Outline each Plasmodium vivax-infected red blood cell.
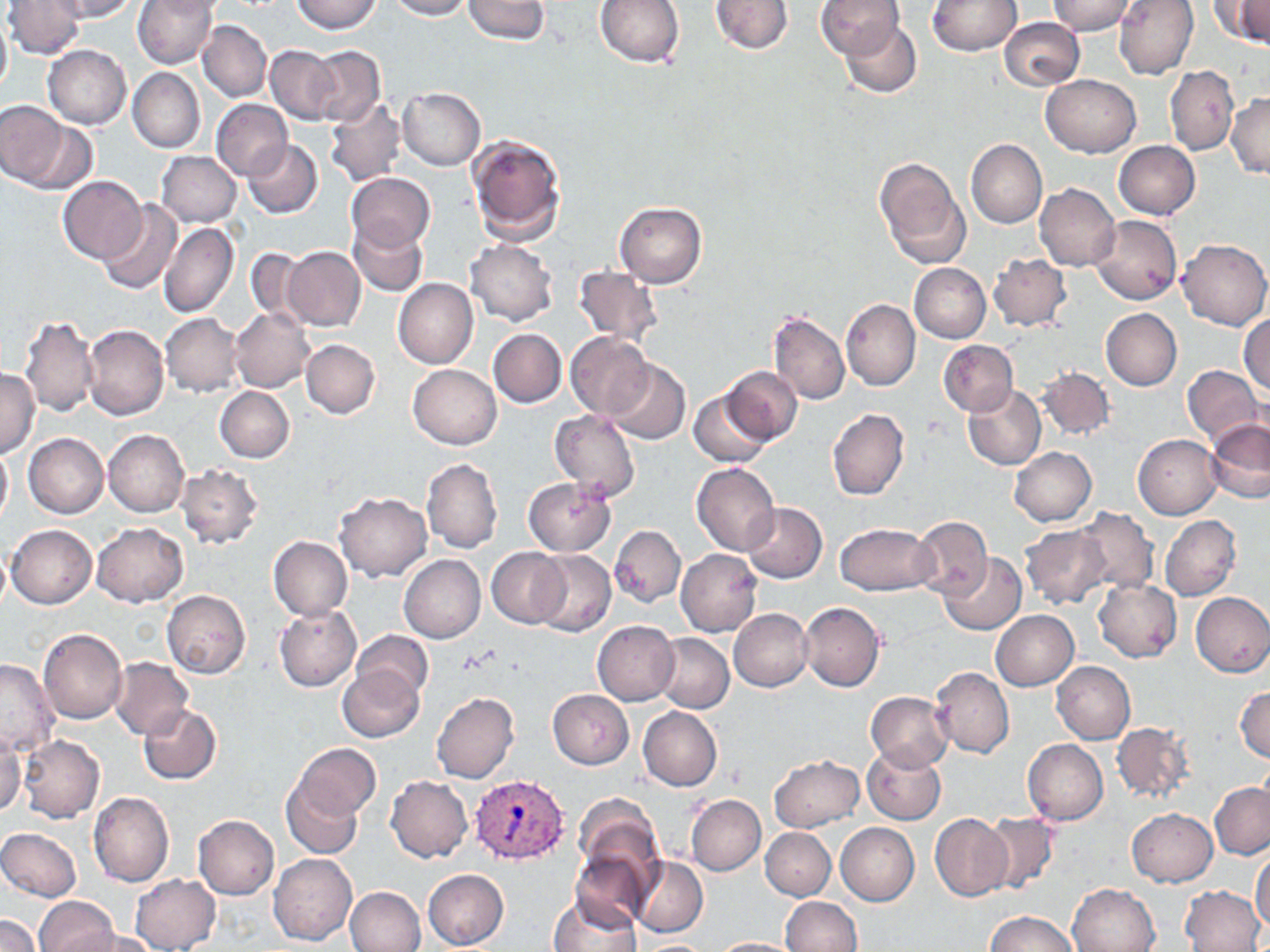

Approximate bounding boxes as (x1,y1)-(x2,y2) corner pairs in pixels.
Plasmodium vivax-infected red blood cells: (470,775)-(570,866).

slide-level diagnosis = Plasmodium vivax
modality = light microscopy
field of view = single
preparation = thin blood smear
uninfected red blood cell locations = approximate bounding boxes as (x1,y1)-(x2,y2) corner pairs in pixels: (4,0)-(84,58), (57,0)-(141,21), (133,0)-(218,69), (290,0)-(381,33), (388,0)-(472,20), (463,0)-(548,43), (595,0)-(685,68), (710,0)-(794,55), (816,0)-(906,59), (927,0)-(1021,55), (1114,0)-(1199,79), (1214,0)-(1270,46), (1048,1)-(1138,35), (0,13)-(11,98), (839,17)-(923,99), (999,18)-(1085,90), (197,20)-(272,102), (42,45)-(132,128), (266,45)-(341,125), (308,46)-(385,127), (1165,65)-(1239,156), (128,67)-(205,153), (1042,74)-(1140,157), (397,88)-(485,170), (1227,92)-(1269,179), (325,98)-(407,187), (210,99)-(292,181), (0,101)-(70,186), (16,119)-(101,195), (466,132)-(566,242), (242,138)-(322,218), (966,140)-(1047,229), (1114,141)-(1200,220), (156,151)-(241,227), (874,157)-(970,269), (345,172)-(435,252), (57,175)-(146,262), (1035,183)-(1121,271), (97,200)-(182,295), (614,201)-(706,287), (1089,214)-(1182,304), (349,220)-(427,295), (159,221)-(238,319), (1177,239)-(1270,331), (467,240)-(558,326), (245,247)-(313,326), (282,247)-(366,331), (989,254)-(1071,330), (909,263)-(990,343), (573,266)-(662,347), (392,278)-(478,369), (842,299)-(920,391), (230,308)-(314,391), (1100,309)-(1181,390), (768,310)-(849,405), (160,313)-(241,396), (1239,313)-(1269,395), (19,315)-(99,416), (83,323)-(168,420), (489,329)-(567,407), (565,332)-(654,419), (301,340)-(380,418), (938,340)-(1018,416), (604,360)-(689,444), (408,364)-(501,449), (1182,364)-(1266,446), (0,367)-(39,459), (723,367)-(803,445), (1036,367)-(1114,441), (962,384)-(1046,470), (215,386)-(293,463), (689,391)-(771,469), (828,408)-(908,500), (549,410)-(640,503), (1205,419)-(1270,503), (103,429)-(189,517), (24,432)-(109,518), (1134,434)-(1223,519), (0,443)-(12,528), (1009,447)-(1096,526), (422,458)-(502,554), (692,463)-(779,556), (176,465)-(264,548), (523,477)-(616,556), (335,492)-(431,581), (741,502)-(828,582), (1074,506)-(1159,595), (910,515)-(992,600), (1161,515)-(1241,602), (91,523)-(187,607), (835,523)-(938,595), (7,524)-(97,609), (1020,525)-(1112,610), (609,526)-(685,607), (268,536)-(353,620), (0,542)-(11,617), (486,547)-(570,628), (676,549)-(762,636), (531,551)-(615,636), (937,553)-(1025,635), (398,555)-(485,643), (1093,578)-(1183,663), (162,591)-(250,678), (1191,592)-(1270,677), (800,602)-(886,692), (275,604)-(361,691), (729,608)-(813,691), (991,611)-(1079,690), (593,621)-(680,705), (39,628)-(127,724), (352,630)-(434,702), (654,632)-(734,712), (108,658)-(194,740), (0,659)-(59,755), (1051,661)-(1135,744), (338,665)-(424,742), (931,666)-(1014,758), (1235,685)-(1270,762), (548,689)-(633,768), (431,692)-(518,783), (866,692)-(952,770), (138,703)-(221,785), (638,706)-(721,791), (1112,721)-(1195,804), (0,732)-(26,818), (17,735)-(105,823), (1023,739)-(1109,825), (292,743)-(380,821), (863,745)-(945,824), (770,755)-(864,832), (386,776)-(473,863), (282,779)-(365,860), (1210,782)-(1269,859), (88,790)-(173,887), (574,794)-(664,882), (687,795)-(765,876), (1126,808)-(1217,887), (930,813)-(1014,901), (982,813)-(1060,893), (193,815)-(280,899), (836,822)-(919,905), (761,827)-(835,900), (0,828)-(82,901), (570,851)-(653,932), (1251,851)-(1270,932), (268,853)-(358,946), (630,856)-(708,936), (422,868)-(508,950), (130,874)-(221,952), (1067,882)-(1160,952), (1181,885)-(1265,952), (344,886)-(425,952), (546,895)-(641,952), (780,896)-(862,952), (34,897)-(118,952), (987,910)-(1078,952), (0,915)-(39,952), (77,929)-(160,952), (710,937)-(804,951), (638,941)-(709,951)
image size = 1270×952 pixels
magnification = 1000x
stain = May-Grünwald-Giemsa